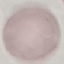

{
  "malaria_status": "uninfected",
  "stain": "Giemsa",
  "capture": "smartphone through the microscope eyepiece",
  "image_type": "automatically extracted cell patch, resized to 64 × 64 pixels",
  "preparation": "thin blood smear"
}